Report the malaria status of this cell.
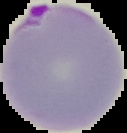
It is parasitized.

image size = 127×133 pixels
image type = segmented cell region with the area outside set to black
preparation = thin blood smear